Identify the blood parasite species.
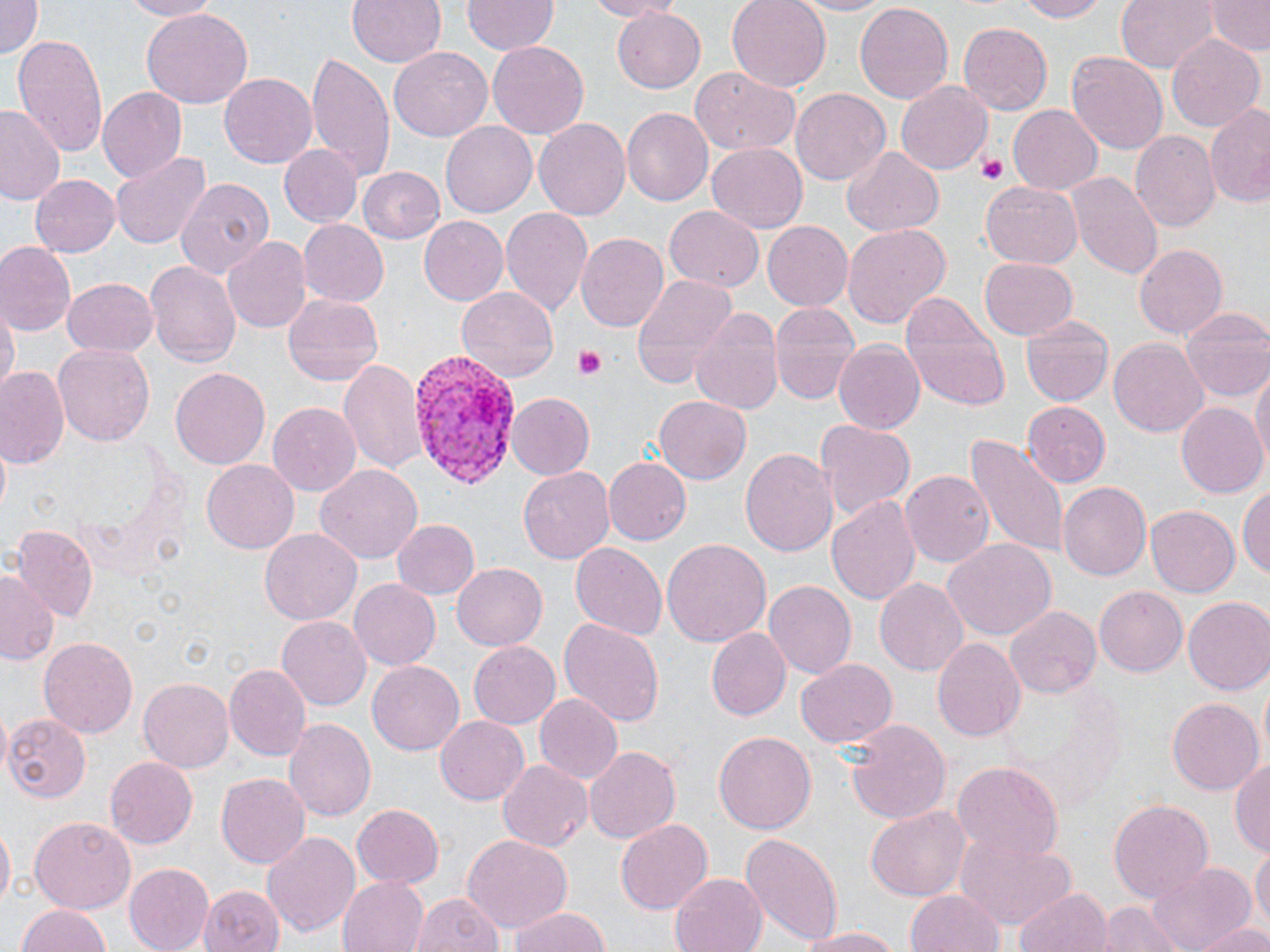

Plasmodium vivax.

magnification = 1000x
Plasmodium vivax-infected red blood cell locations = approximate bounding boxes as (x1,y1)-(x2,y2) corner pairs in pixels: (405,352)-(520,487)
image size = 1270×952 pixels
platelet locations = approximate bounding boxes as (x1,y1)-(x2,y2) corner pairs in pixels: (975,151)-(1008,186), (574,347)-(608,380)
uninfected red blood cell locations = approximate bounding boxes as (x1,y1)-(x2,y2) corner pairs in pixels: (115,0)-(221,20), (349,0)-(446,68), (580,0)-(678,20), (726,0)-(829,90), (787,0)-(899,18), (1012,0)-(1109,22), (1116,0)-(1217,74), (0,1)-(43,58), (461,1)-(557,55), (854,1)-(955,105), (1206,1)-(1268,55), (141,8)-(251,111), (612,9)-(706,93), (959,22)-(1052,114), (13,33)-(109,156), (1168,34)-(1264,133), (485,40)-(591,141), (388,46)-(494,142), (1067,51)-(1168,157), (304,53)-(396,178), (690,68)-(801,156), (219,72)-(317,169), (896,78)-(993,172), (99,88)-(187,183), (789,88)-(891,185), (1204,103)-(1270,207), (0,104)-(67,205), (1008,104)-(1102,195), (622,106)-(714,204), (534,118)-(630,222), (440,122)-(536,219), (1132,131)-(1221,233), (705,142)-(808,233), (281,144)-(361,226), (842,147)-(946,237), (108,150)-(213,250), (359,166)-(445,243), (1068,171)-(1162,279), (29,174)-(119,259), (175,175)-(275,278), (980,181)-(1082,268), (501,205)-(595,321), (663,207)-(764,291), (419,216)-(509,306), (297,219)-(389,307), (762,221)-(853,311), (843,224)-(951,328), (577,233)-(669,334), (221,236)-(310,334), (1,244)-(75,335), (1135,244)-(1228,341), (979,257)-(1077,338), (146,260)-(240,366), (629,272)-(739,386), (62,278)-(157,359), (456,286)-(560,381), (899,289)-(1010,408), (283,294)-(384,386), (2,299)-(18,398), (769,299)-(862,404), (689,302)-(786,418), (1182,307)-(1270,402), (1022,316)-(1114,405), (834,337)-(925,433), (1109,338)-(1206,436), (53,342)-(154,447), (339,357)-(428,477), (1252,365)-(1269,470), (170,366)-(271,470), (1,369)-(68,467), (507,392)-(595,478), (654,395)-(751,485), (1022,401)-(1112,489), (266,402)-(363,495), (1177,402)-(1268,499), (816,420)-(914,521), (963,431)-(1071,561), (0,443)-(12,511), (740,447)-(836,560), (602,456)-(690,546), (200,459)-(299,554), (316,465)-(423,561), (518,466)-(615,564), (900,470)-(994,569), (1057,480)-(1151,581), (1238,480)-(1268,584), (827,495)-(922,605), (1146,507)-(1239,596), (392,518)-(479,600), (11,528)-(96,622), (260,528)-(361,624), (661,538)-(770,648), (944,539)-(1054,640), (569,542)-(666,639), (453,564)-(547,649), (0,567)-(58,663), (874,576)-(969,677), (349,579)-(441,670), (765,580)-(857,679), (1093,585)-(1187,677), (1184,597)-(1270,695), (1005,604)-(1100,698), (276,616)-(371,710), (558,617)-(665,729), (709,627)-(790,721), (39,637)-(137,738), (931,637)-(1025,744), (469,640)-(560,727), (797,659)-(897,748), (368,660)-(465,756), (223,664)-(309,759), (138,678)-(234,773), (534,693)-(624,785), (1167,696)-(1263,793), (1,715)-(94,803), (435,715)-(530,805), (284,718)-(376,823), (843,718)-(950,827), (714,731)-(816,834), (584,746)-(683,843), (1230,753)-(1270,858), (104,756)-(198,850), (497,758)-(593,854), (951,761)-(1063,865), (215,773)-(309,870), (1108,799)-(1213,904), (351,802)-(444,888), (866,805)-(972,901), (30,816)-(136,914), (616,817)-(712,913), (0,825)-(14,912), (955,829)-(1076,929), (262,831)-(360,940), (740,831)-(843,944), (461,834)-(571,935), (1253,843)-(1268,935), (1147,857)-(1257,949), (125,863)-(212,951), (670,871)-(770,951), (338,874)-(428,952), (203,882)-(282,952), (1015,887)-(1112,952), (908,890)-(1004,952), (411,891)-(505,952), (1101,900)-(1189,952), (16,903)-(116,952), (505,907)-(613,952), (1192,920)-(1269,952), (792,926)-(907,950)
stain = May-Grünwald-Giemsa
modality = optical microscopy
field of view = single
preparation = thin blood smear